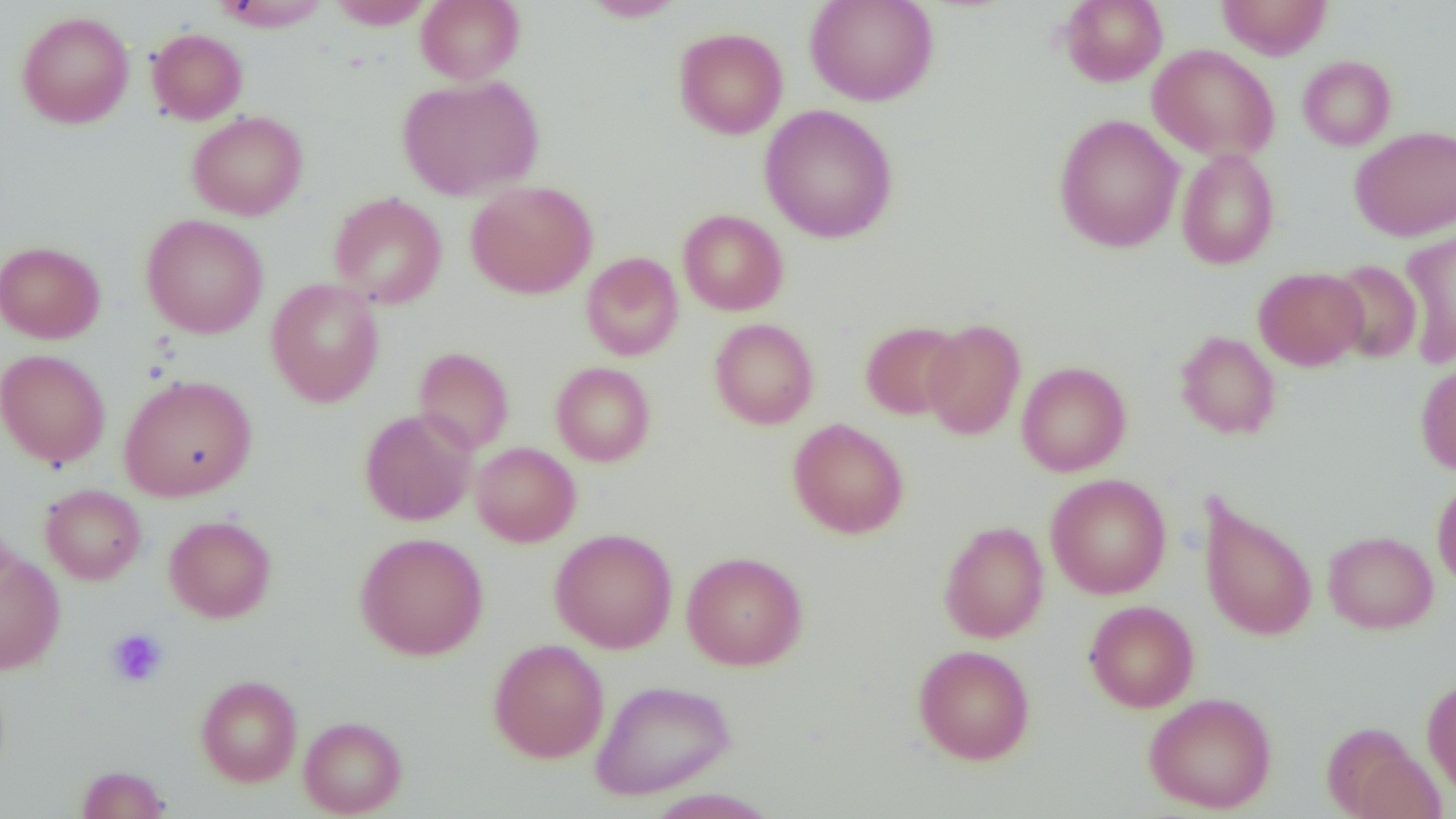 Approximate bounding boxes as (x1,y1)-(x2,y2) corner pairs in pixels. Uninfected red blood cell locations: (212,0)-(332,31), (416,0)-(525,84), (581,0)-(686,21), (805,0)-(938,106), (1058,0)-(1168,87), (1216,0)-(1333,59), (327,1)-(434,29), (16,11)-(134,128), (674,27)-(788,139), (147,28)-(248,125), (1148,44)-(1280,162), (1297,55)-(1396,150), (397,75)-(543,200), (759,104)-(899,244), (187,111)-(308,220), (1053,114)-(1184,252), (1350,125)-(1456,241), (1176,147)-(1280,270), (466,180)-(597,299), (329,192)-(447,310), (678,209)-(788,316), (141,214)-(269,339), (1399,227)-(1456,367), (0,241)-(105,343), (581,252)-(683,361), (1326,259)-(1422,363), (1254,267)-(1367,370), (265,278)-(384,407), (709,319)-(818,429), (921,319)-(1026,441), (859,321)-(965,420), (1175,330)-(1280,439), (413,347)-(514,455), (0,349)-(111,468), (1415,359)-(1456,474), (1016,361)-(1131,476), (550,362)-(656,466), (118,374)-(257,501), (359,408)-(477,526), (788,418)-(909,539), (470,442)-(581,547), (1046,473)-(1171,599), (1432,476)-(1456,591), (40,484)-(146,585), (1197,496)-(1318,641), (164,515)-(276,623), (938,521)-(1049,643), (550,528)-(678,653), (1323,531)-(1438,634), (355,532)-(488,660), (0,551)-(65,674), (682,552)-(808,671), (1084,600)-(1199,712), (488,638)-(609,763), (913,644)-(1035,764), (196,675)-(302,787), (1422,676)-(1456,797), (591,679)-(736,800), (1143,692)-(1277,813), (299,716)-(407,817), (1345,744)-(1446,819), (75,765)-(170,819). Platelet locations: (106,628)-(168,687). Slide-level diagnosis: no evidence of blood parasites. Single field of view. Image is 1456×819 pixels. Thin blood smear. 1000x magnification. Light microscopy.